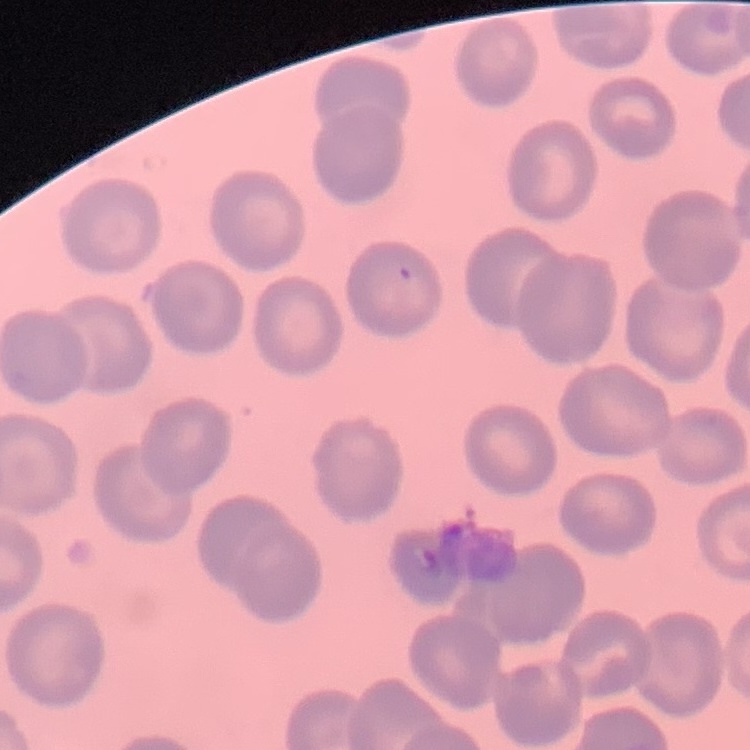 The erythrocytes show no rouleaux formation. Stained with either Field's or Giemsa. Thin blood film. One tile cut from a larger photomicrograph.